Assess this cell for malaria.
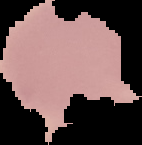
Uninfected.

Summary:
  - Image size: 142×145 pixels
  - Image type: cell region segmented out of the field of view; surrounding area masked to black
  - Preparation: thin blood smear